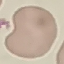
result = no malaria parasites seen
capture = smartphone through the microscope eyepiece
preparation = thin blood smear
stain = Giemsa
image type = cell patch, automatically extracted from a larger field of view and resized to 64 × 64 pixels